Classify this cell by malaria status.
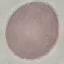

It is uninfected.

stain: Giemsa
capture: smartphone camera at the microscope eyepiece
preparation: thin smear
image_type: automatically extracted cell patch, resized to 64 × 64 pixels